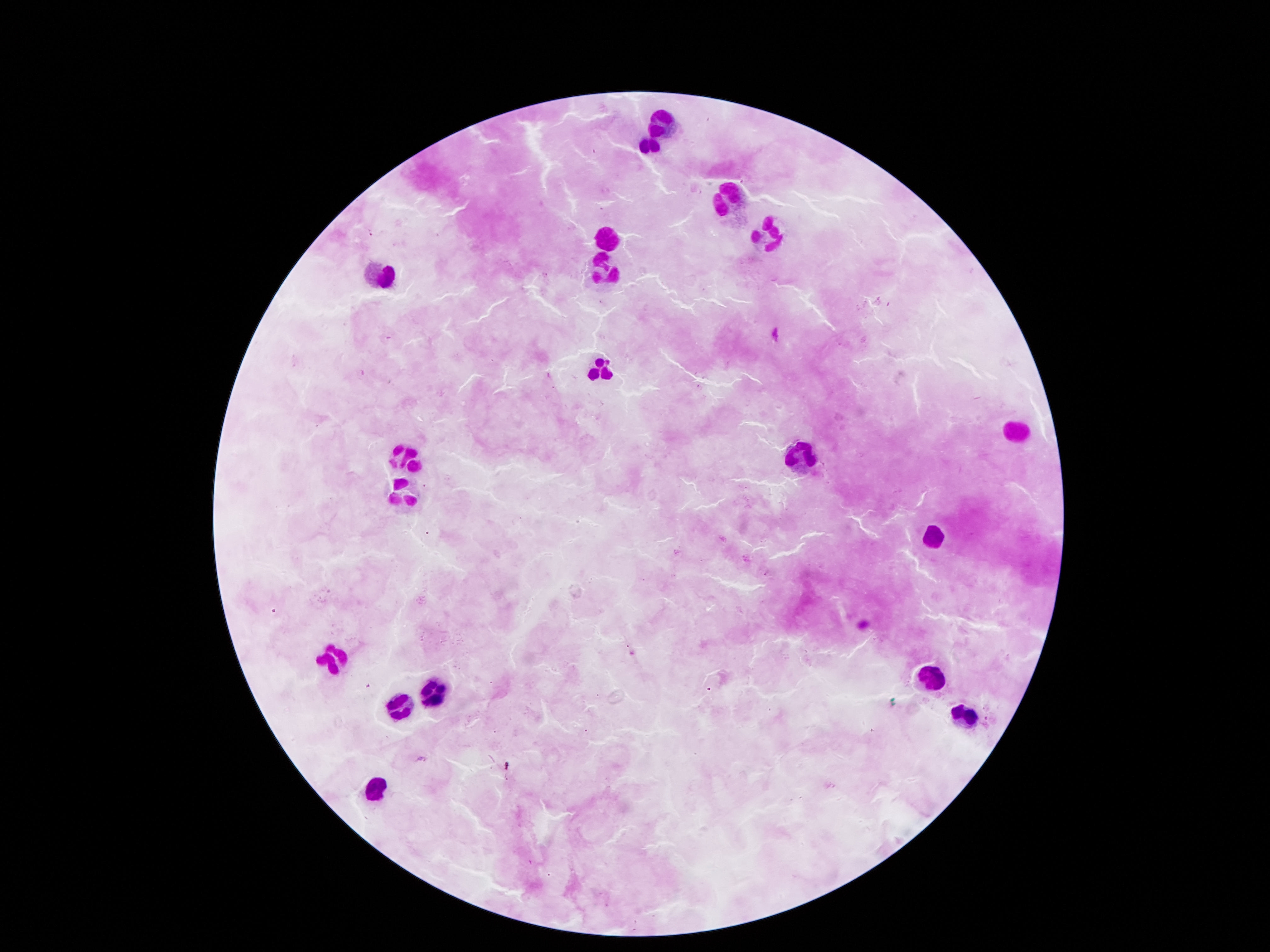
stain = Giemsa
image size = 1270×952 pixels
patient malaria status = negative
field of view = one from this slide
preparation = thick blood smear
capture = smartphone camera through the microscope eyepiece
magnification = 100x
leukocyte locations = approximate centers as (x, y) in pixels: (665, 122), (650, 144), (723, 200), (767, 235), (602, 243), (604, 267), (380, 275), (600, 373), (1013, 434), (408, 453), (794, 458), (404, 490), (935, 538), (333, 657), (929, 678), (434, 691), (397, 705), (965, 718), (373, 793)